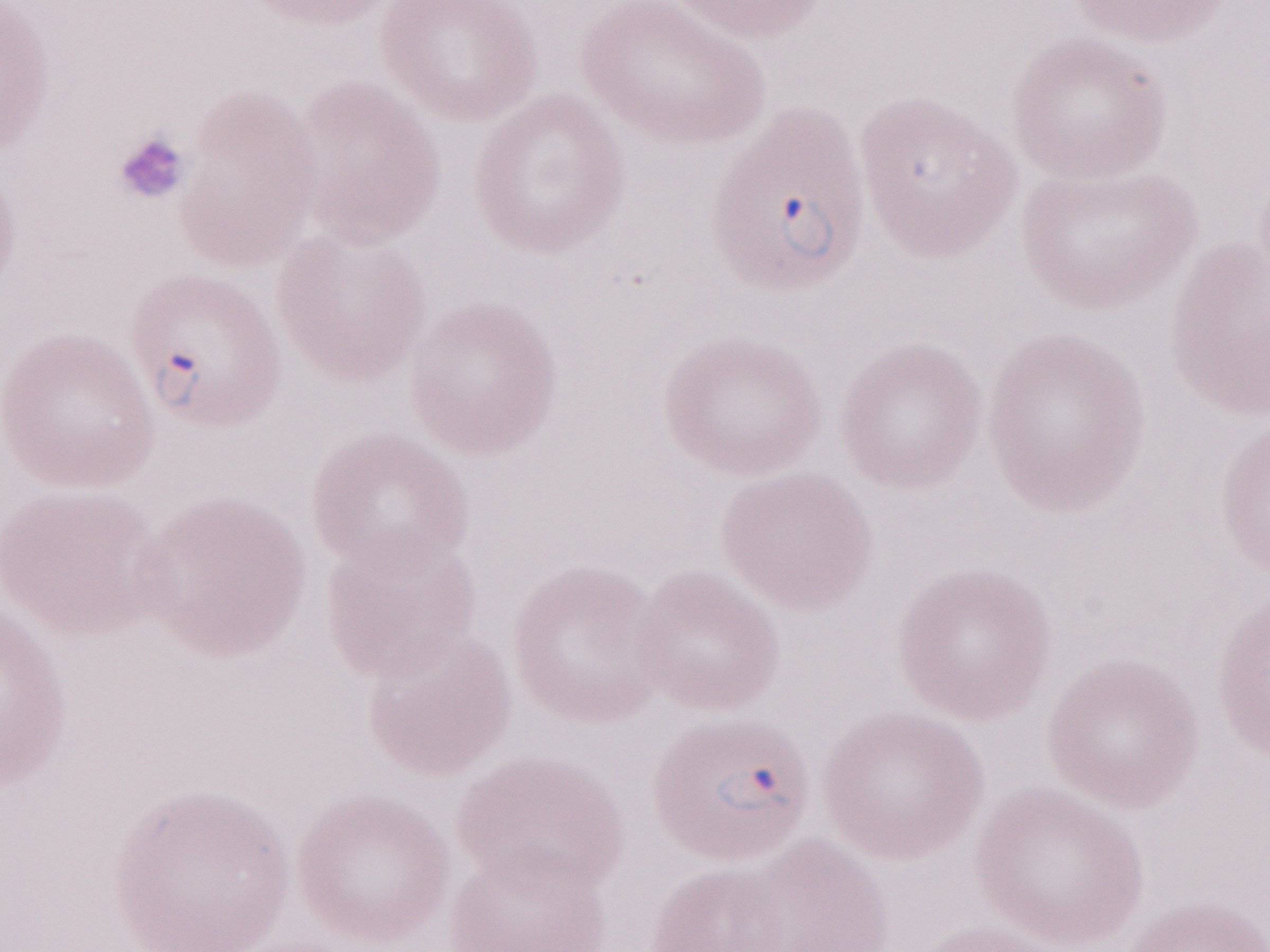

May-Grünwald-Giemsa (MGG) stain. 1,000x magnification. One field of this slide. Olympus BX43 microscope and DP73 digital camera. Image is 1270×952 pixels. Thin blood smear. Patient diagnosis: malaria infection.